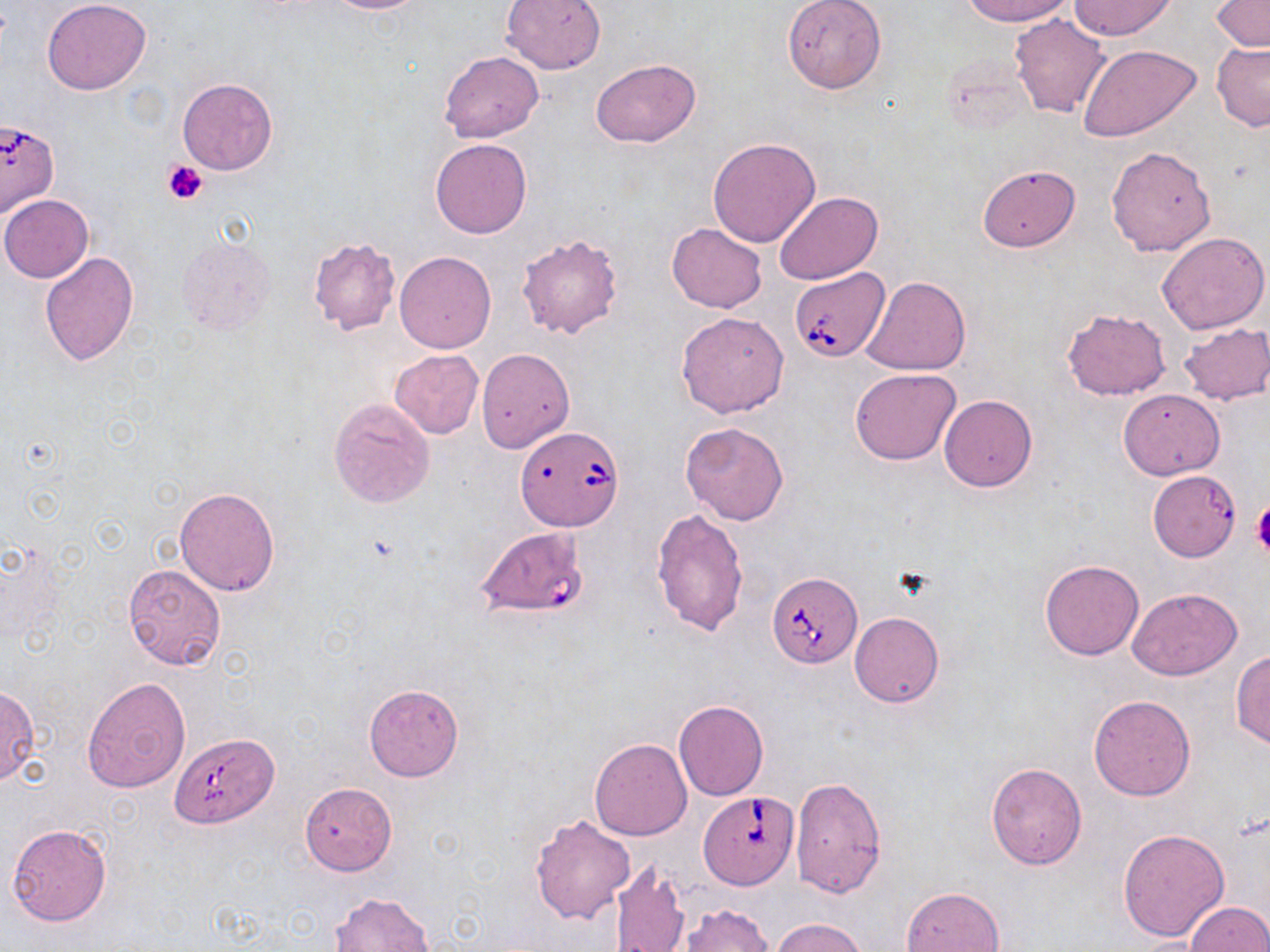
slide-level diagnosis = Babesia divergens
uninfected red blood cell locations = approximate bounding boxes as (x1,y1)-(x2,y2) corner pairs in pixels: (42,0)-(150,95), (320,0)-(433,13), (501,0)-(604,74), (781,0)-(887,94), (961,0)-(1075,25), (1211,0)-(1270,51), (1070,1)-(1174,39), (1009,12)-(1111,118), (1211,41)-(1270,132), (1078,44)-(1202,143), (440,50)-(544,142), (590,57)-(701,148), (177,77)-(278,175), (708,137)-(821,247), (430,138)-(532,238), (1106,146)-(1216,256), (976,164)-(1081,252), (774,190)-(883,284), (0,194)-(94,282), (667,223)-(766,313), (1158,230)-(1270,334), (517,233)-(625,339), (177,237)-(277,336), (308,237)-(401,335), (394,251)-(496,353), (39,252)-(139,364), (861,276)-(970,376), (1061,307)-(1172,400), (676,311)-(789,417), (1178,323)-(1270,405), (476,348)-(574,453), (388,349)-(485,439), (850,368)-(961,465), (1118,387)-(1224,479), (939,395)-(1037,491), (328,397)-(435,508), (679,421)-(790,525), (174,486)-(280,596), (652,508)-(749,636), (1039,559)-(1143,660), (123,564)-(226,670), (1127,587)-(1242,679), (850,612)-(944,707), (1230,649)-(1270,751), (82,677)-(191,793), (364,684)-(463,780), (0,687)-(40,785), (1089,695)-(1195,801), (673,699)-(769,801), (590,738)-(693,840), (985,763)-(1087,868), (790,777)-(887,897), (300,783)-(396,875), (529,814)-(634,923), (7,823)-(111,927), (1117,828)-(1230,942), (608,857)-(691,952), (901,887)-(1004,952), (329,891)-(436,952), (1185,902)-(1270,951), (678,904)-(773,951), (771,917)-(870,952)
image size = 1270×952 pixels
magnification = 1000x
modality = optical microscopy
preparation = thin blood film
platelet locations = approximate bounding boxes as (x1,y1)-(x2,y2) corner pairs in pixels: (163,159)-(208,205), (1250,503)-(1270,557)
field of view = single
stain = May-Grünwald-Giemsa
Babesia divergens-infected red blood cell locations = approximate bounding boxes as (x1,y1)-(x2,y2) corner pairs in pixels: (0,119)-(59,219), (788,268)-(890,362), (516,426)-(622,531), (1147,470)-(1241,562), (476,528)-(586,617), (766,571)-(862,668), (171,734)-(277,828), (698,789)-(797,890)